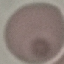 Malaria status: uninfected. Thin blood smear. Acquired by smartphone through the microscope eyepiece. Cell patch, automatically extracted from a larger field of view and resized to 64 × 64 pixels. Giemsa stain.